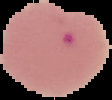
Summary:
  - Malaria status: parasitized
  - Image type: segmented cell region with the area outside set to black
  - Image size: 112×100 pixels
  - Preparation: thin blood film